Point out each Plasmodium parasite.
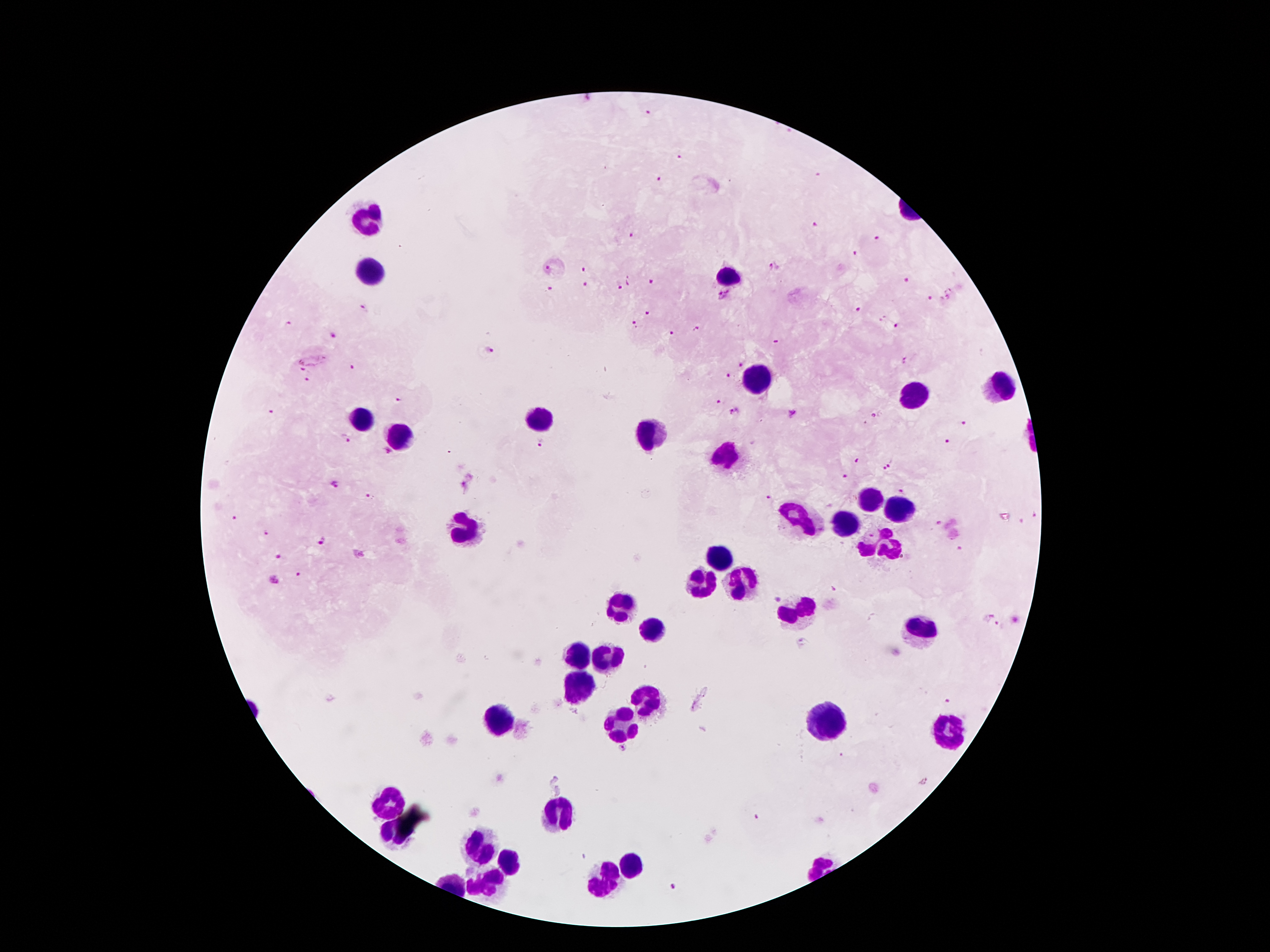
Approximate centers as {x, y} in pixels.
Plasmodium parasites: {586, 100}, {649, 113}, {679, 157}, {660, 179}, {816, 226}, {631, 234}, {877, 238}, {856, 254}, {549, 268}, {774, 268}, {585, 271}, {629, 279}, {907, 281}, {650, 282}, {587, 285}, {620, 285}, {551, 289}, {725, 295}, {930, 298}, {950, 298}, {362, 307}, {858, 311}, {648, 314}, {633, 324}, {898, 327}, {695, 329}, {671, 333}, {336, 337}, {775, 343}, {489, 349}, {310, 357}, {908, 360}, {739, 365}, {352, 367}, {729, 375}, {310, 381}, {399, 399}, {719, 402}, {736, 410}, {273, 413}, {794, 413}, {878, 413}, {965, 421}, {345, 438}, {949, 440}, {540, 441}, {389, 453}, {856, 461}, {891, 463}, {883, 470}, {846, 476}, {338, 486}, {463, 489}, {904, 491}, {769, 497}, {367, 499}, {1034, 514}, {233, 520}, {939, 523}, {268, 534}, {323, 541}, {961, 549}, {359, 554}, {278, 557}, {297, 575}, {276, 580}, {834, 588}, {778, 598}, {986, 617}, {1000, 626}, {800, 645}, {950, 703}, {694, 707}, {622, 749}, {926, 782}, {754, 819}, {672, 890}.

Leukocyte locations: {363, 217}, {374, 274}, {729, 279}, {756, 385}, {997, 389}, {913, 397}, {359, 418}, {538, 420}, {649, 435}, {395, 439}, {729, 456}, {869, 500}, {890, 511}, {798, 519}, {842, 527}, {466, 530}, {882, 544}, {718, 559}, {739, 582}, {699, 586}, {617, 608}, {798, 612}, {653, 631}, {916, 633}, {578, 651}, {605, 658}, {575, 687}, {651, 700}, {500, 717}, {823, 721}, {619, 723}, {951, 728}, {386, 803}, {559, 815}, {483, 841}, {510, 866}, {630, 866}, {603, 879}, {487, 889}. Thick blood smear. Patient malaria status: positive for Plasmodium falciparum. Smartphone photograph taken through the microscope eyepiece. Single field of view. Image is 1270×952 pixels. Giemsa-stained preparation. 100x magnification.